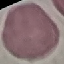
result = no malaria parasites detected
capture = smartphone camera at the microscope eyepiece
preparation = thin blood film
image type = automatically extracted cell patch, resized to 64 × 64 pixels
stain = Giemsa